Identify the preparation type.
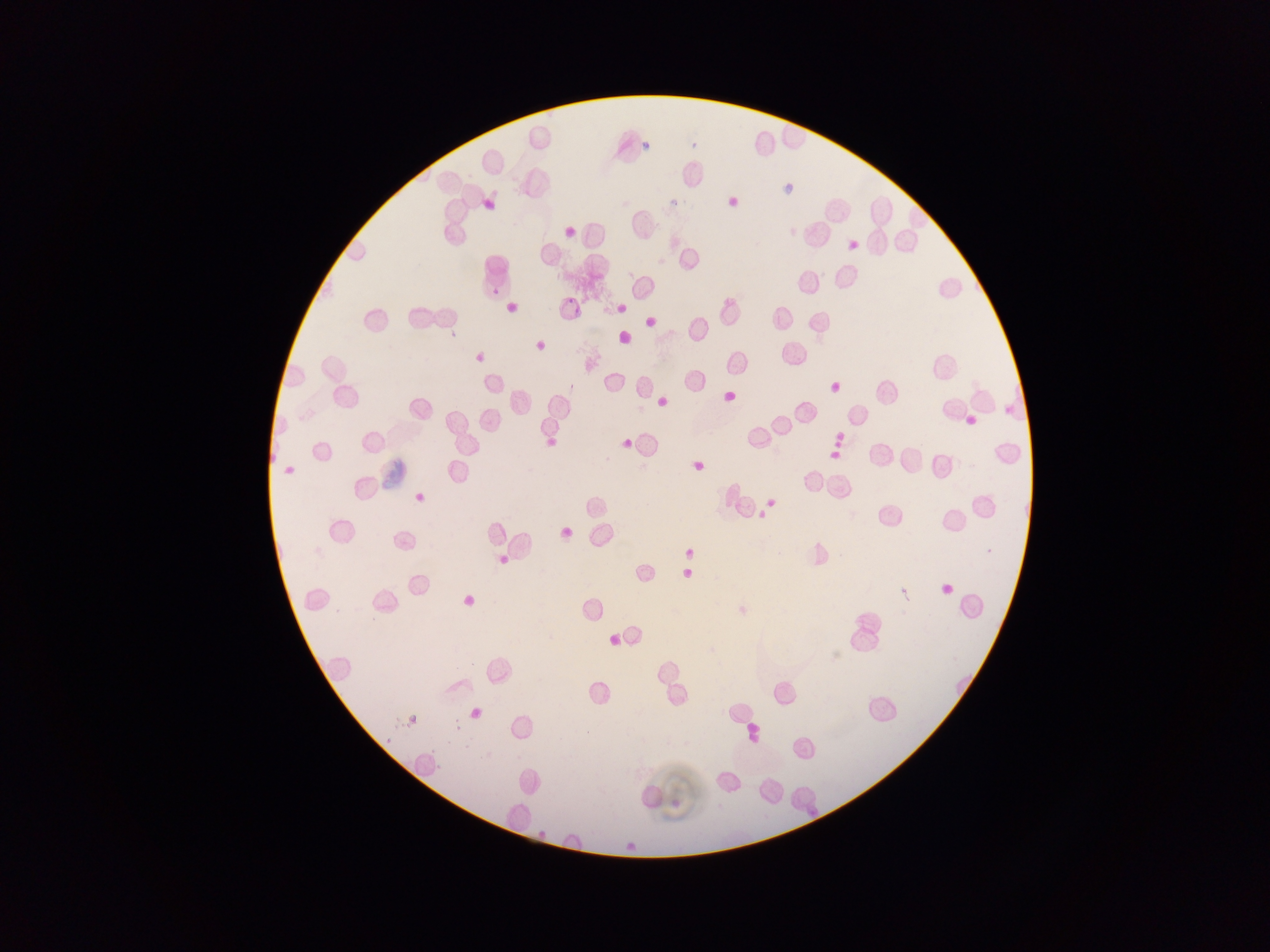

This is a thin smear.

field of view = single
capture = mobile-phone photograph through a microscope
country = Ghana
image size = 1270×952 pixels
malaria parasite locations = approximate bounding boxes as {left, top, right, bottom} in pixels: {490, 286, 500, 297}, {566, 293, 575, 304}, {569, 300, 583, 317}, {445, 324, 459, 343}, {983, 546, 994, 556}, {388, 713, 404, 729}, {449, 719, 463, 733}, {381, 734, 392, 755}, {427, 741, 441, 762}, {430, 759, 444, 777}, {809, 807, 817, 815}